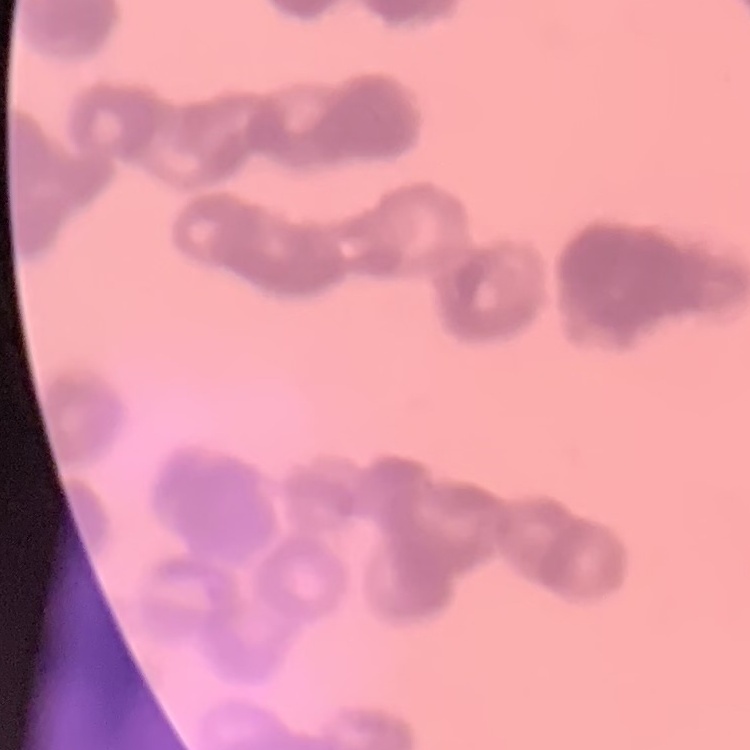
red blood cell morphology = rouleaux formation
stain = Field's or Giemsa
preparation = thin peripheral smear
image type = square crop of a larger photomicrograph